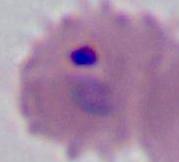

Summary:
  - Magnification: 400x or 1000x
  - Modality: photomicrograph
  - Identification: Plasmodium